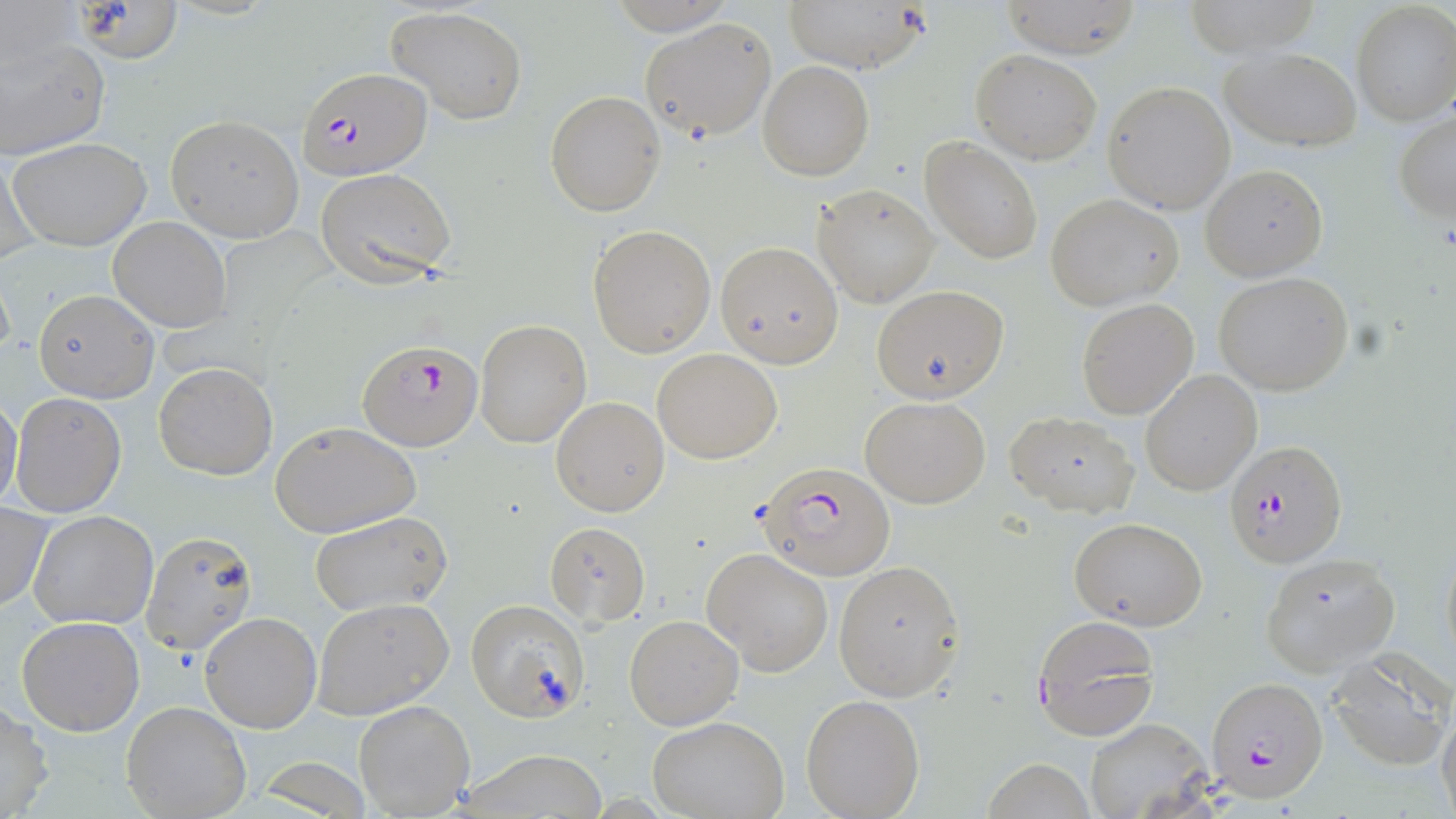
plasmodium_falciparum_infected_red_blood_cell_locations: 'approximate bounding boxes as named x1/y1/x2/y2 corners in pixels: (x1=294, y1=66, x2=432, y2=182), (x1=358, y1=339, x2=483, y2=451), (x1=1227, y1=440, x2=1348, y2=567), (x1=758, y1=460, x2=898, y2=582), (x1=1031, y1=614, x2=1160, y2=741), (x1=1205, y1=676, x2=1329, y2=802)'
slide_level_diagnosis: Plasmodium falciparum
preparation: thin blood film
field_of_view: one of a larger specimen
stain: May-Grünwald-Giemsa
image_size: 1456×819 pixels
magnification: 1000x
modality: optical microscopy
uninfected_red_blood_cell_locations: 'approximate bounding boxes as named x1/y1/x2/y2 corners in pixels: (x1=782, y1=0, x2=928, y2=73), (x1=1000, y1=0, x2=1143, y2=59), (x1=1181, y1=0, x2=1324, y2=57), (x1=1351, y1=3, x2=1456, y2=126), (x1=385, y1=5, x2=527, y2=125), (x1=639, y1=17, x2=778, y2=143), (x1=0, y1=33, x2=110, y2=162), (x1=1223, y1=47, x2=1361, y2=152), (x1=972, y1=49, x2=1102, y2=163), (x1=758, y1=60, x2=874, y2=180), (x1=1103, y1=80, x2=1237, y2=215), (x1=544, y1=91, x2=666, y2=215), (x1=1394, y1=111, x2=1456, y2=224), (x1=165, y1=114, x2=305, y2=242), (x1=8, y1=135, x2=153, y2=252), (x1=920, y1=136, x2=1041, y2=265), (x1=1, y1=148, x2=40, y2=271), (x1=1200, y1=164, x2=1328, y2=281), (x1=314, y1=167, x2=457, y2=287), (x1=812, y1=184, x2=939, y2=307), (x1=1047, y1=194, x2=1184, y2=309), (x1=108, y1=216, x2=231, y2=333), (x1=587, y1=224, x2=716, y2=358), (x1=715, y1=240, x2=844, y2=368), (x1=1213, y1=271, x2=1355, y2=395), (x1=872, y1=285, x2=1009, y2=403), (x1=33, y1=289, x2=156, y2=401), (x1=1076, y1=299, x2=1199, y2=420), (x1=475, y1=319, x2=591, y2=448), (x1=653, y1=348, x2=783, y2=463), (x1=153, y1=362, x2=278, y2=481), (x1=1140, y1=369, x2=1262, y2=495), (x1=10, y1=391, x2=127, y2=518), (x1=0, y1=395, x2=23, y2=514), (x1=862, y1=395, x2=990, y2=508), (x1=551, y1=396, x2=669, y2=516), (x1=1006, y1=412, x2=1140, y2=517), (x1=270, y1=421, x2=421, y2=538), (x1=0, y1=503, x2=53, y2=613), (x1=28, y1=509, x2=159, y2=630), (x1=311, y1=511, x2=453, y2=618), (x1=1067, y1=517, x2=1209, y2=632), (x1=545, y1=522, x2=650, y2=628), (x1=142, y1=531, x2=258, y2=655), (x1=1439, y1=538, x2=1455, y2=674), (x1=703, y1=548, x2=834, y2=674), (x1=1261, y1=554, x2=1399, y2=674), (x1=833, y1=560, x2=966, y2=702), (x1=311, y1=597, x2=455, y2=720), (x1=465, y1=600, x2=590, y2=721), (x1=200, y1=611, x2=322, y2=734), (x1=624, y1=614, x2=744, y2=730), (x1=16, y1=617, x2=145, y2=736), (x1=1325, y1=650, x2=1453, y2=769), (x1=800, y1=694, x2=926, y2=818), (x1=0, y1=700, x2=54, y2=819), (x1=353, y1=700, x2=473, y2=815), (x1=121, y1=701, x2=252, y2=818), (x1=1438, y1=705, x2=1456, y2=819), (x1=647, y1=716, x2=790, y2=819), (x1=1086, y1=720, x2=1210, y2=819), (x1=462, y1=748, x2=609, y2=819), (x1=984, y1=757, x2=1093, y2=819)'